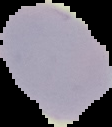
Summary:
  - Result: no malaria parasites detected
  - Image size: 112×127 pixels
  - Image type: segmented cell region on a black background
  - Preparation: thin blood film